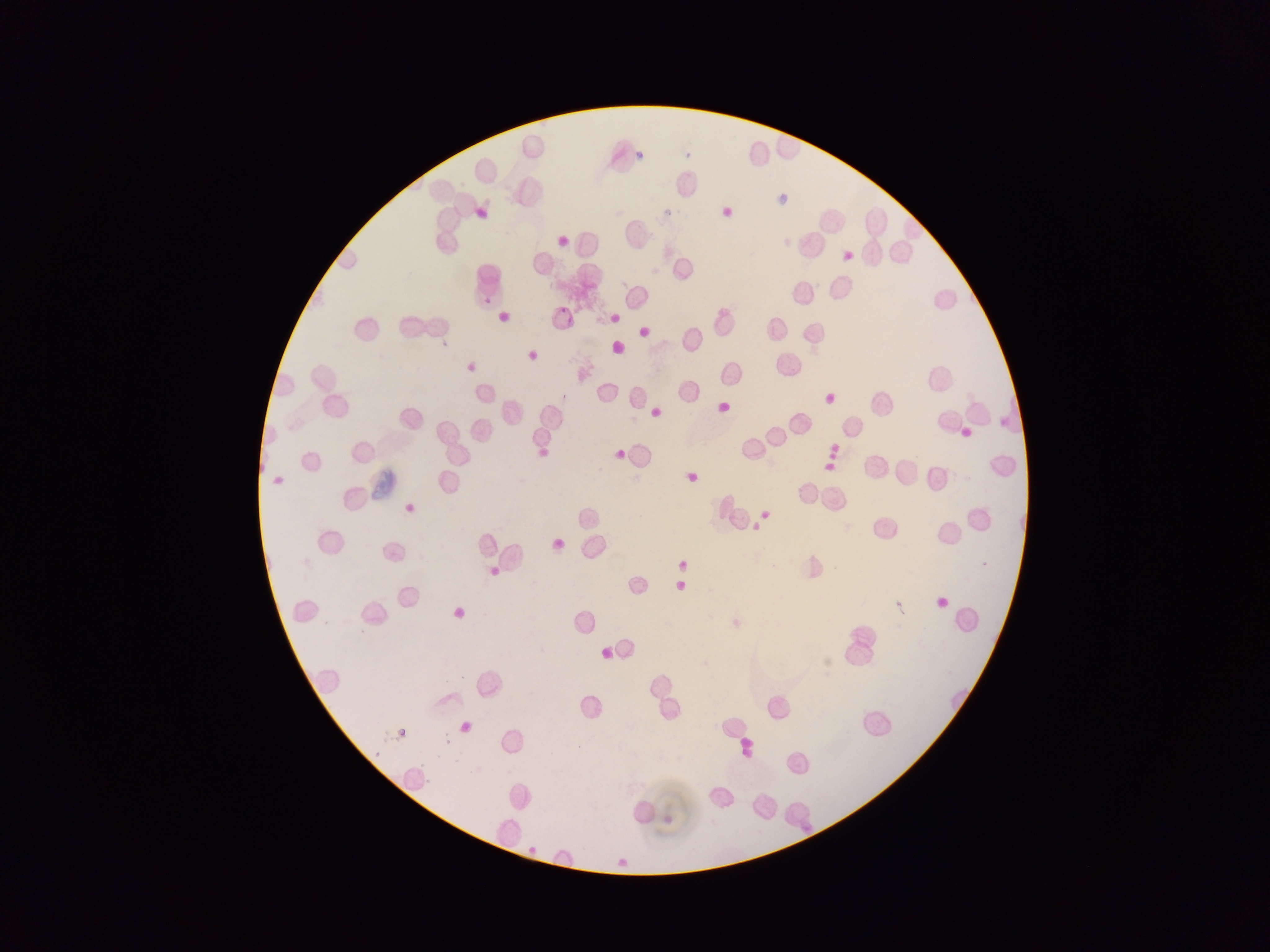

Approximate bounding boxes as left top right bottom in pixels. Plasmodium parasite locations: 636 152 644 160; 478 296 495 307; 557 306 567 313; 564 316 576 327; 397 729 406 740; 444 738 451 746; 802 824 810 833. Sample from Ghana. Image is 1270×952 pixels. Single field of view. Mobile-phone photograph taken through the microscope. Thin blood film.